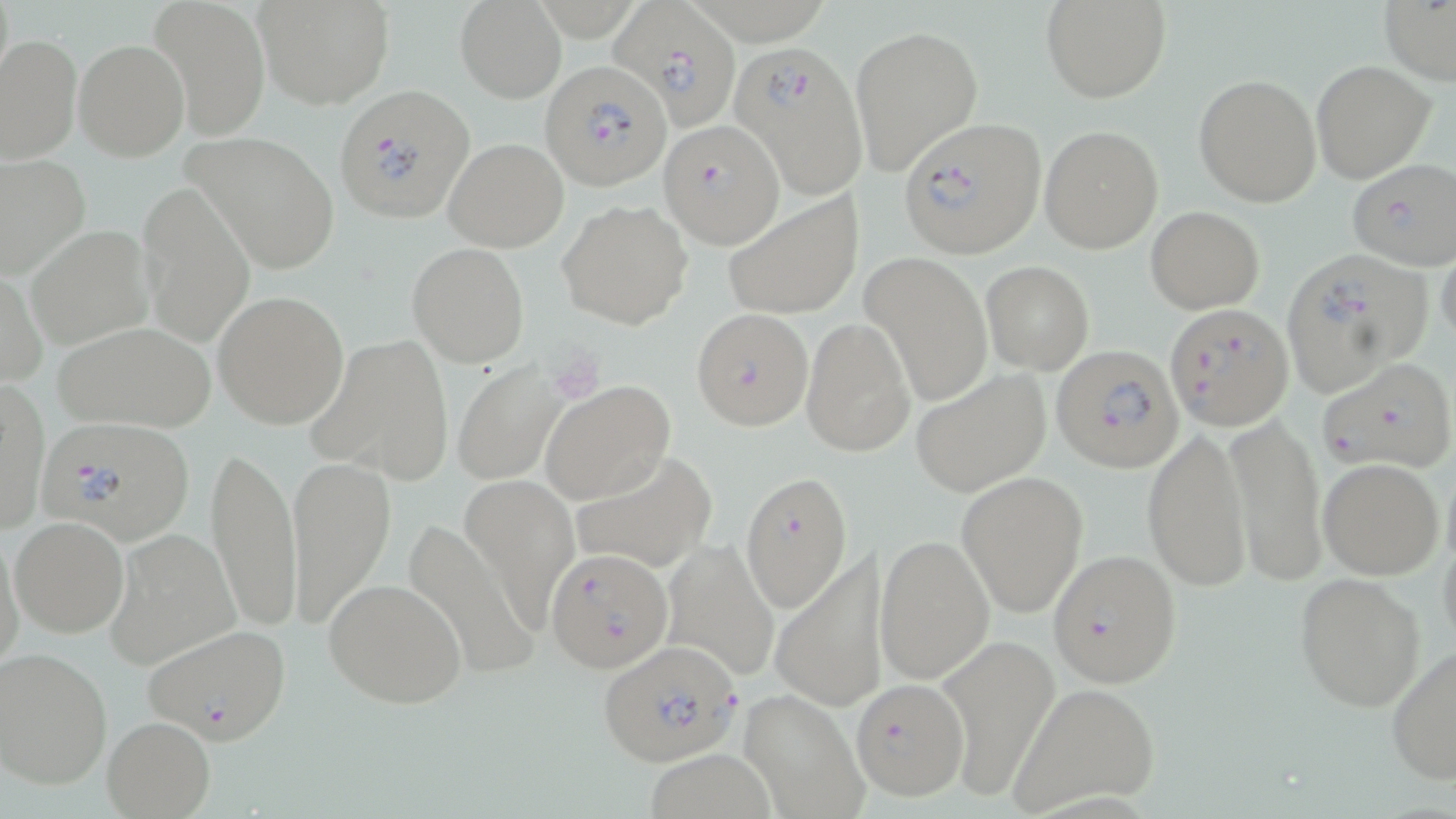 Approximate bounding boxes as (x1,y1)-(x2,y2) corner pairs in pixels. Platelet locations: (548,351)-(606,401). Uninfected red blood cell locations: (150,0)-(270,141), (454,0)-(566,103), (1042,0)-(1169,102), (1379,0)-(1456,87), (255,2)-(393,108), (849,22)-(983,178), (0,35)-(82,164), (73,38)-(189,162), (1310,60)-(1435,182), (1194,73)-(1322,206), (1039,124)-(1164,252), (182,129)-(340,275), (443,138)-(568,252), (0,156)-(89,279), (139,184)-(253,345), (724,194)-(863,321), (557,199)-(694,330), (1146,205)-(1266,313), (28,224)-(155,350), (1436,237)-(1456,354), (407,242)-(530,368), (862,252)-(993,408), (981,260)-(1094,375), (1,269)-(47,389), (213,291)-(350,429), (801,317)-(915,456), (53,322)-(217,432), (308,334)-(455,486), (452,360)-(569,487), (910,368)-(1051,499), (0,380)-(48,534), (540,381)-(677,504), (1226,413)-(1327,585), (1141,428)-(1250,593), (207,442)-(300,627), (569,450)-(714,577), (288,456)-(396,628), (1316,457)-(1445,579), (955,470)-(1088,620), (461,475)-(577,627), (10,516)-(129,639), (399,518)-(539,682), (102,526)-(240,671), (1,528)-(25,678), (874,534)-(994,684), (659,542)-(779,678), (769,549)-(888,715), (1294,572)-(1428,712), (324,576)-(467,708), (143,624)-(292,744), (935,634)-(1060,799), (1386,641)-(1456,784), (0,647)-(113,791), (1006,682)-(1162,815), (738,687)-(868,819), (102,716)-(215,818). Plasmodium falciparum-infected red blood cell locations: (613,1)-(740,132), (728,38)-(867,197), (542,60)-(667,190), (337,84)-(477,224), (899,117)-(1045,258), (660,118)-(781,245), (1346,159)-(1456,271), (1279,249)-(1434,401), (1163,302)-(1293,432), (690,308)-(814,430), (1051,346)-(1185,473), (1317,355)-(1456,477), (35,415)-(197,543), (738,472)-(852,615), (546,548)-(672,673), (1047,548)-(1182,688), (597,639)-(741,767), (850,678)-(970,800). Slide-level diagnosis: Plasmodium falciparum. Thin blood smear. Image is 1456×819 pixels. May-Grünwald-Giemsa stain. Single field of view. Optical microscopy. Captured at 1000x magnification.